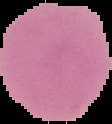
From a thin blood smear. Cell region segmented out of the field of view; the surrounding area is masked to black. Image is 112×124 pixels. Malaria status: uninfected.